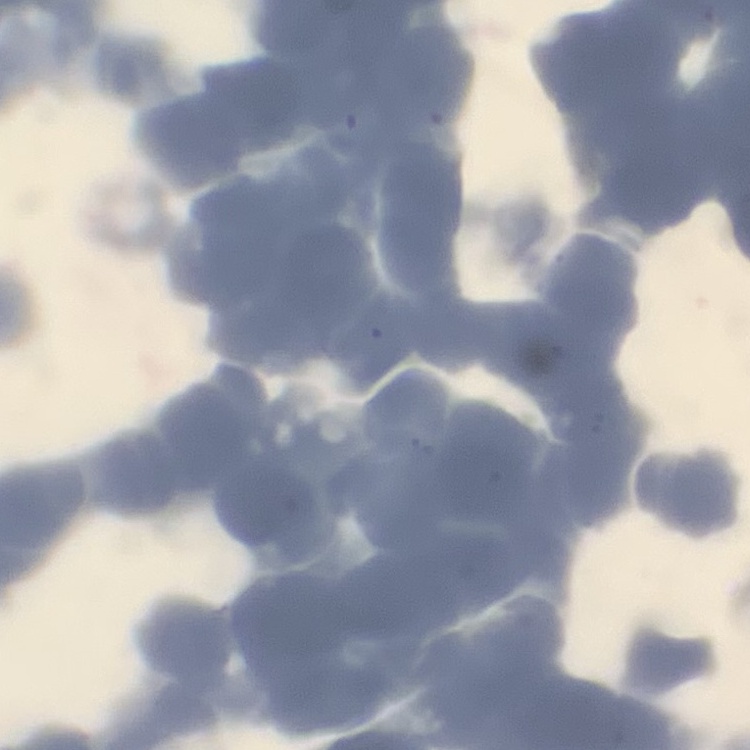

{
  "red_blood_cell_morphology": "rouleaux formation",
  "preparation": "thin blood smear",
  "image_type": "one tile cut from a larger photomicrograph",
  "stain": "Field's or Giemsa"
}